Describe the morphology of the red blood cells.
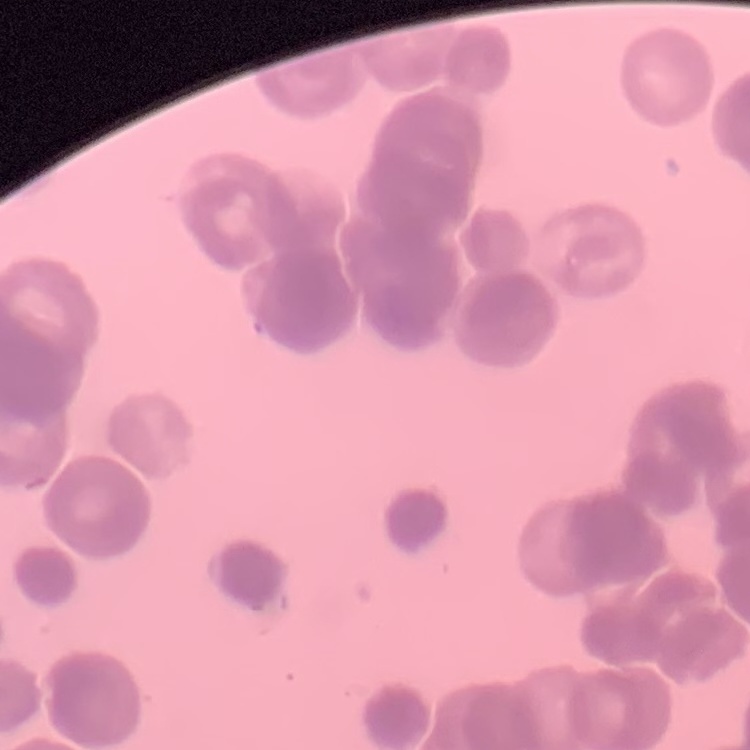
Rouleaux formation.

image type = one tile cut from a larger photomicrograph
stain = Field's or Giemsa
preparation = thin blood film